Identify the parasite.
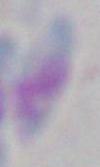
This is Toxoplasma gondii.

Summary:
  - Magnification: 1000x
  - Modality: micrograph